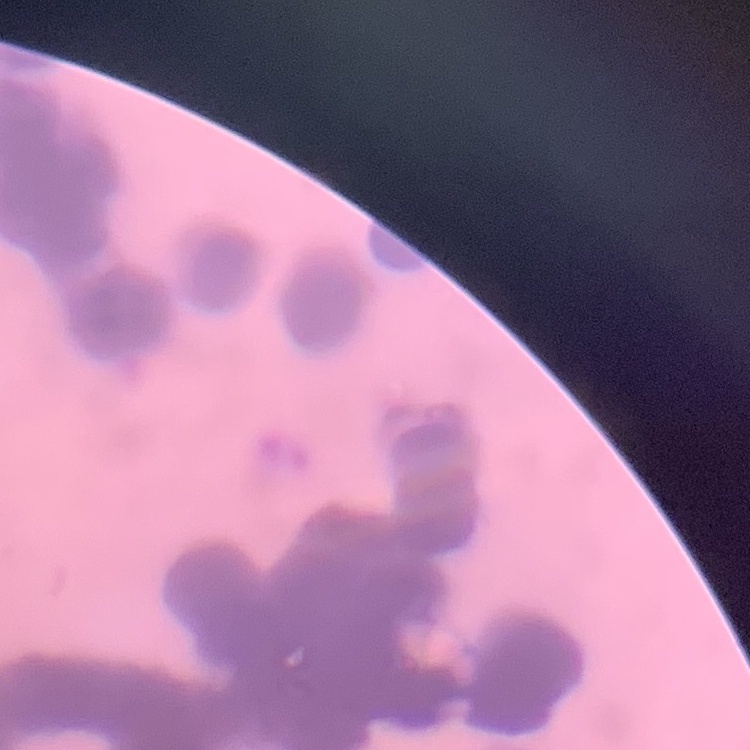

Summary:
  - Erythrocyte morphology: rouleaux formation
  - Stain: Field's or Giemsa
  - Preparation: thin blood film
  - Image type: one tile cut from a larger photomicrograph